Name the parasite shown.
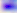
Toxoplasma gondii.

magnification = 400x
modality = photomicrograph